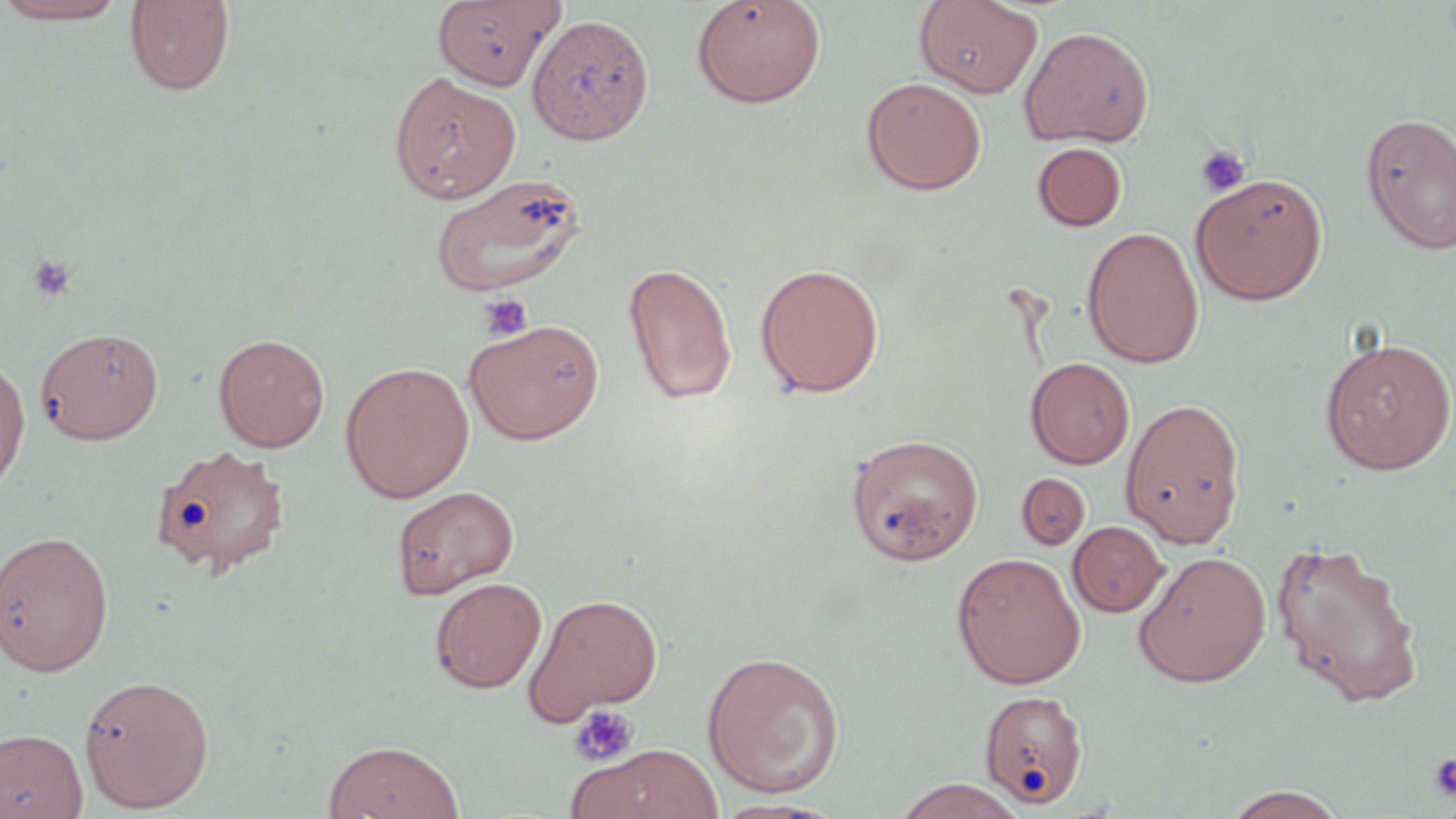

Summary:
  - Coordinate format: approximate bounding boxes as (x1,y1)-(x2,y2) corner pairs in pixels
  - Uninfected red blood cell locations: (0,0)-(130,24), (124,0)-(235,95), (433,0)-(563,90), (691,0)-(826,107), (914,1)-(1043,98), (527,13)-(654,146), (1019,26)-(1154,147), (389,71)-(521,203), (862,77)-(987,195), (1360,112)-(1456,255), (1033,141)-(1127,231), (1191,173)-(1328,304), (429,174)-(587,298), (1082,226)-(1204,368), (623,260)-(737,405), (754,262)-(885,397), (462,318)-(604,444), (35,326)-(163,444), (213,333)-(330,452), (1319,338)-(1456,474), (0,355)-(31,495), (1026,357)-(1135,469), (339,361)-(475,502), (1121,397)-(1247,548), (846,434)-(983,565), (150,444)-(291,578), (1016,473)-(1091,551), (391,485)-(519,598), (1068,521)-(1168,617), (0,530)-(114,677), (1272,540)-(1424,706), (1133,551)-(1271,686), (952,552)-(1087,689), (429,577)-(546,693), (524,593)-(664,723), (701,651)-(845,798), (78,674)-(215,812), (979,689)-(1090,809), (0,729)-(88,819), (323,741)-(465,819), (568,744)-(725,819), (892,778)-(1028,819), (1219,785)-(1351,818), (709,797)-(842,818)
  - Platelet locations: (1195,145)-(1251,197), (28,255)-(77,301), (479,294)-(533,342), (569,704)-(639,767), (1429,752)-(1456,801)
  - Slide-level diagnosis: negative for blood parasites
  - Field of view: one of a larger specimen
  - Modality: optical microscopy
  - Stain: May-Grünwald-Giemsa
  - Magnification: 1000x
  - Preparation: thin blood smear
  - Image size: 1456×819 pixels